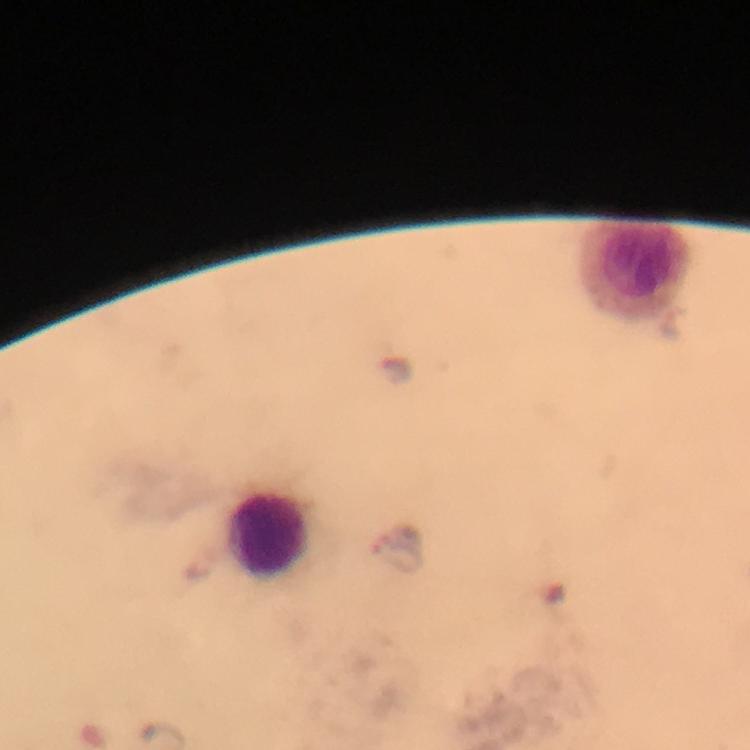 Approximate centers as (x, y) in pixels. Leukocyte locations: (635, 269), (265, 534). Thick smear. Image is 750×750 pixels. At 100x magnification. A crop from one field of view. Giemsa-stained preparation. Immersion oil was used. Photographed through the microscope with a smartphone camera. Malaria parasites: none detected. From a diagnostic examination for malaria.